Point out each malaria parasite and classify it by life-cycle stage.
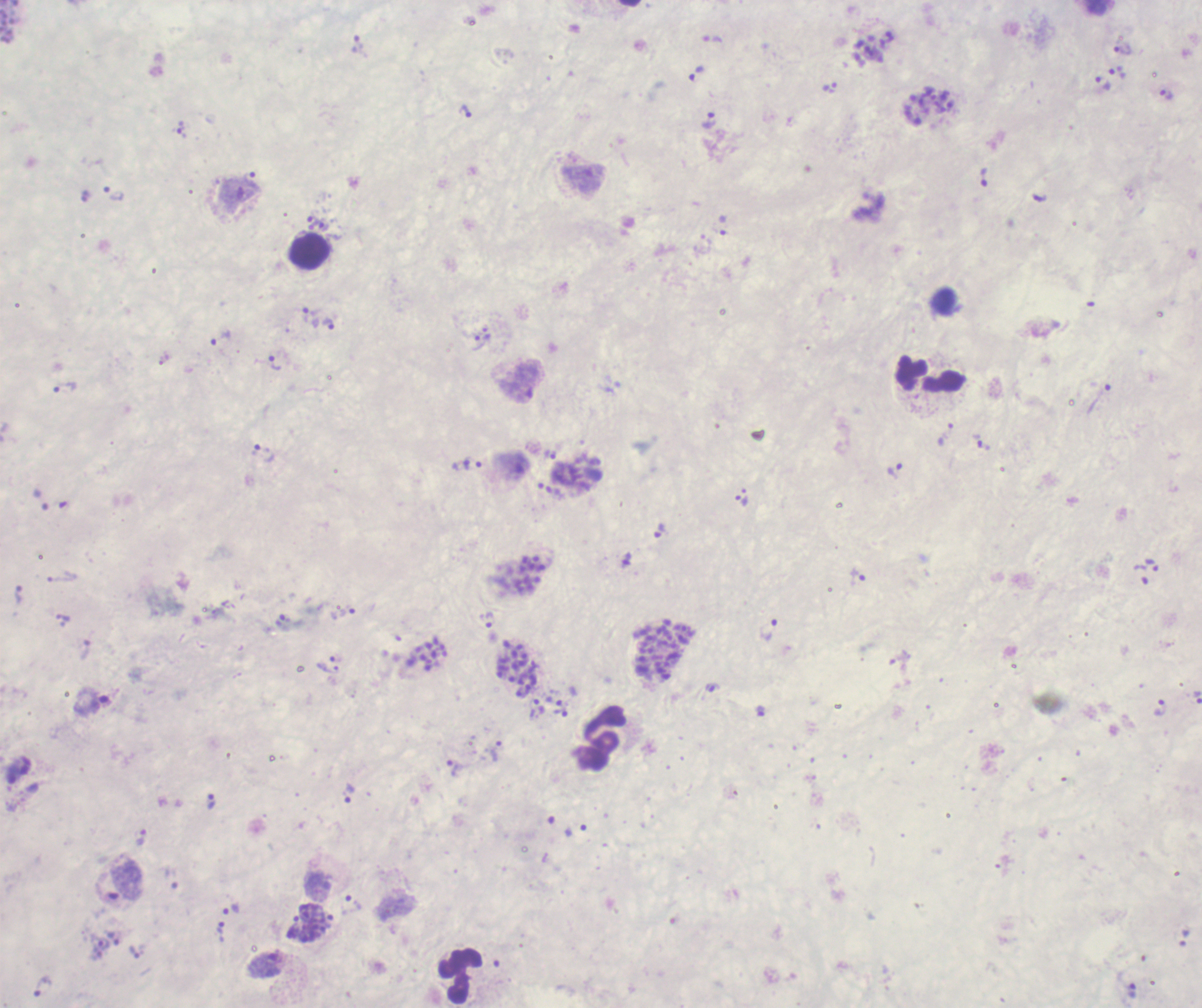

Approximate centers as (x, y) in pixels.
Trophozoites: (358, 45), (1123, 50), (1118, 72), (696, 74), (1103, 84), (829, 87), (1166, 95), (465, 112), (709, 120), (182, 130), (984, 178), (114, 194), (313, 221), (324, 227), (311, 311), (329, 324), (219, 338), (275, 362), (65, 389), (982, 442), (263, 453), (551, 455), (473, 464), (894, 470), (741, 501), (659, 531), (1152, 564), (1141, 574), (858, 578), (347, 611), (63, 617), (490, 619), (284, 622), (769, 631), (712, 687), (1197, 697), (92, 702), (1160, 707), (538, 708), (760, 711), (560, 712), (496, 752), (452, 767), (350, 793), (211, 801), (141, 837), (354, 904), (232, 911), (293, 927), (221, 932), (102, 943), (135, 952), (266, 963), (44, 987).
Schizonts: (931, 107), (528, 575), (663, 651), (431, 656), (518, 669), (316, 924).
No gametocyte forms observed.

{
  "background_quality": "unsatisfactory",
  "preparation": "thick blood smear",
  "coloration_quality": "bad",
  "context": "previously used in an actual diagnosis",
  "leukocyte_locations": "approximate centers as (x, y) in pixels: (310, 251), (931, 372), (601, 738), (460, 975)",
  "image_size": "1202×1008 pixels",
  "stain": "Romanowsky",
  "field_of_view": "one from this slide",
  "magnification": "100x"
}